Describe the morphology of the erythrocytes.
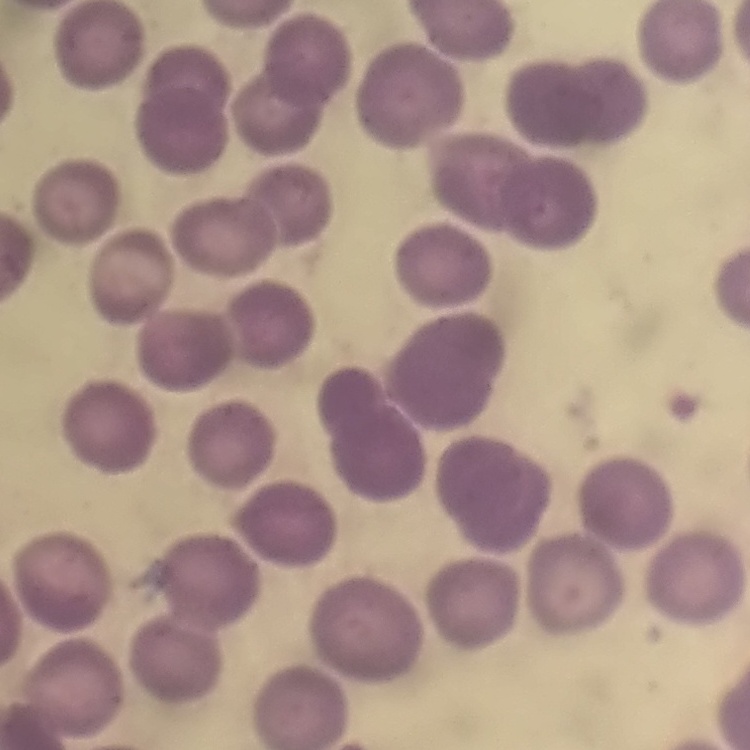
No rouleaux formation.

One tile cut from a larger photomicrograph. Thin blood smear. Stained with either Field's or Giemsa.